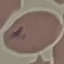

Malaria status: parasitized. Giemsa-stained preparation. Thin smear of blood. Automatically extracted cell patch, resized to 64 × 64 pixels. Acquired by smartphone through the microscope eyepiece.